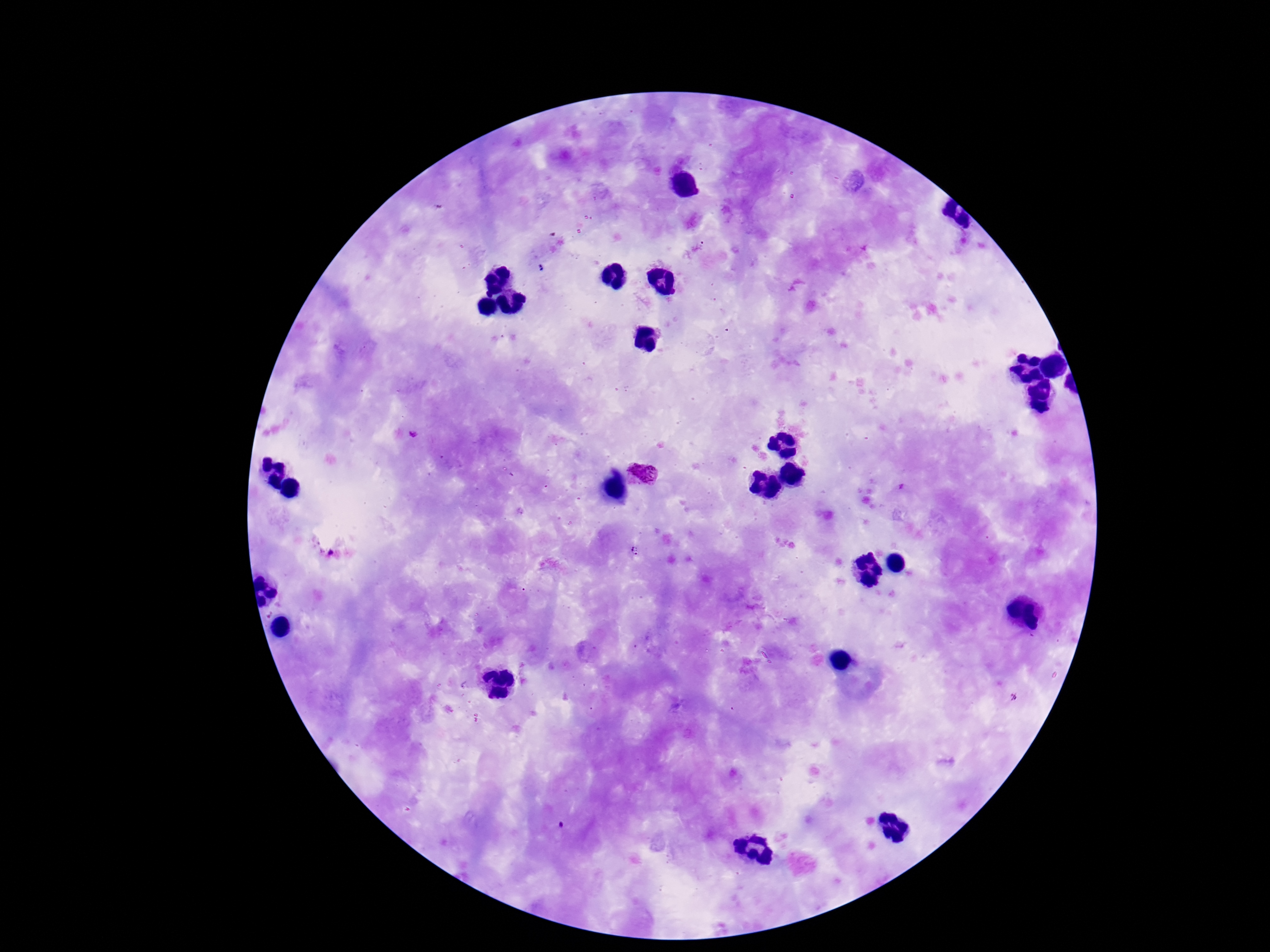

Approximate centers as (x, y) in pixels.
Summary:
  - Plasmodium parasite locations: (696, 248), (413, 434), (645, 471), (633, 551)
  - Stain: Giemsa
  - Patient malaria status: positive
  - Field of view: single
  - Preparation: thick peripheral-blood smear
  - Image size: 1270×952 pixels
  - Capture: smartphone camera through the microscope eyepiece
  - Magnification: 100x